Give the extent of all Plasmodium malariae-infected red blood cells.
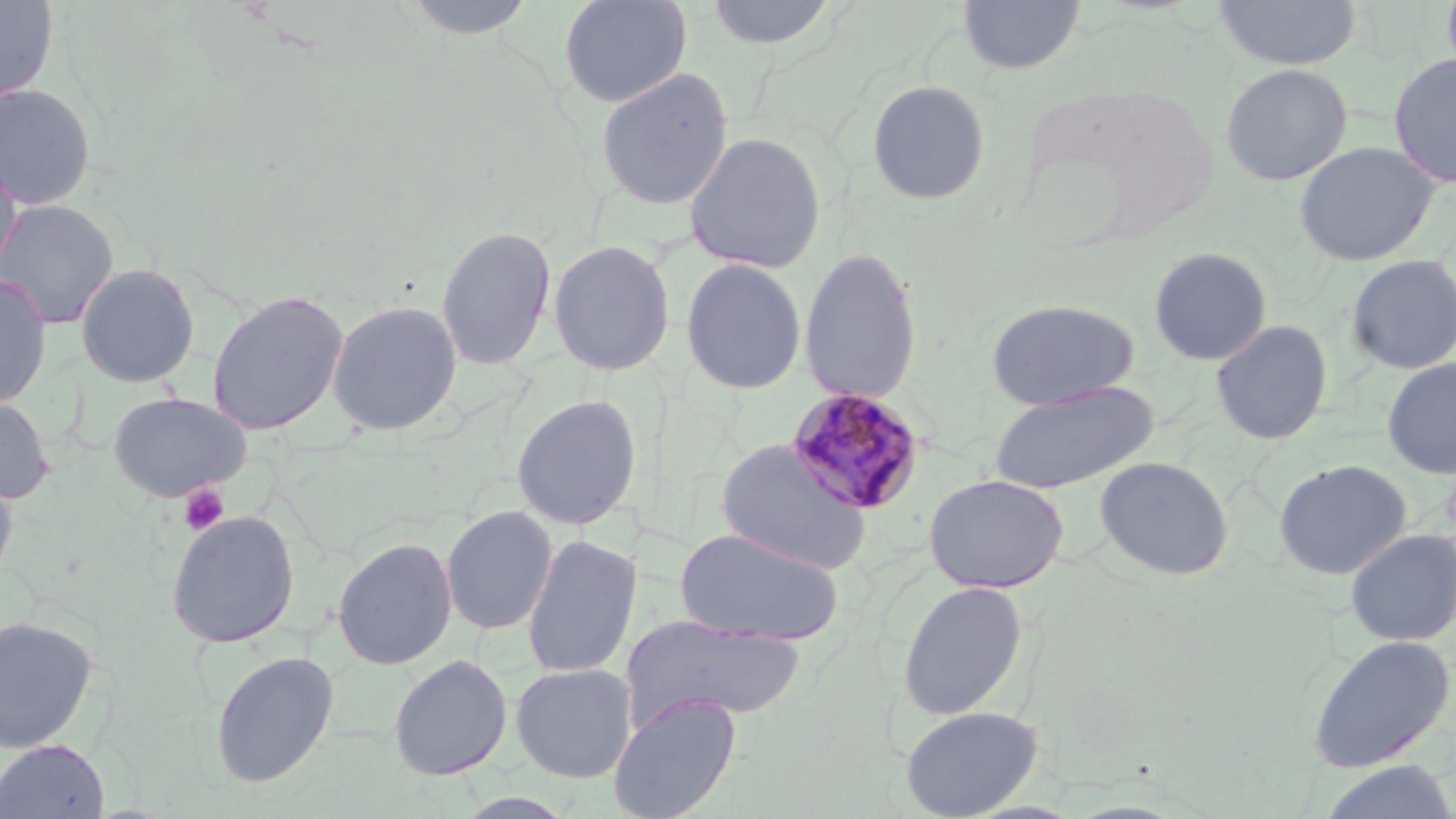
Approximate bounding boxes as (x1, y1, x2, y2) in pixels.
Plasmodium malariae-infected red blood cells: (786, 387, 925, 515).

slide-level diagnosis = Plasmodium malariae
modality = light microscopy
platelet locations = approximate bounding boxes as (x1, y1, x2, y2) in pixels: (177, 482, 230, 535)
preparation = thin blood film
image size = 1456×819 pixels
stain = May-Grünwald-Giemsa
uninfected red blood cell locations = approximate bounding boxes as (x1, y1, x2, y2) in pixels: (0, 0, 59, 103), (399, 0, 540, 40), (558, 0, 692, 108), (704, 0, 838, 51), (957, 0, 1085, 74), (1212, 0, 1362, 70), (1388, 52, 1456, 188), (1220, 62, 1353, 186), (595, 66, 733, 211), (866, 79, 992, 206), (0, 82, 97, 210), (683, 131, 827, 274), (1294, 140, 1441, 267), (0, 151, 23, 279), (0, 198, 120, 331), (435, 224, 557, 371), (548, 239, 676, 376), (798, 246, 923, 406), (1148, 246, 1272, 365), (1346, 254, 1456, 375), (680, 257, 807, 394), (74, 261, 201, 388), (0, 272, 52, 410), (206, 288, 350, 436), (985, 298, 1138, 410), (326, 299, 463, 436), (1210, 319, 1333, 445), (1381, 357, 1456, 479), (989, 381, 1157, 495), (107, 391, 251, 503), (0, 394, 56, 505), (511, 394, 642, 530), (715, 438, 872, 575), (1094, 456, 1233, 581), (1273, 459, 1412, 580), (0, 465, 19, 595), (925, 474, 1068, 594), (441, 505, 558, 635), (165, 509, 301, 648), (673, 527, 844, 647), (1344, 528, 1456, 646), (521, 533, 642, 679), (332, 536, 457, 671), (896, 579, 1029, 722), (0, 613, 99, 754), (624, 614, 805, 726), (1305, 633, 1456, 773), (209, 649, 340, 788), (388, 654, 512, 781), (511, 662, 637, 782), (608, 694, 741, 819), (899, 705, 1043, 818), (0, 739, 111, 819), (1317, 760, 1456, 819)
magnification = 1000x
field of view = single